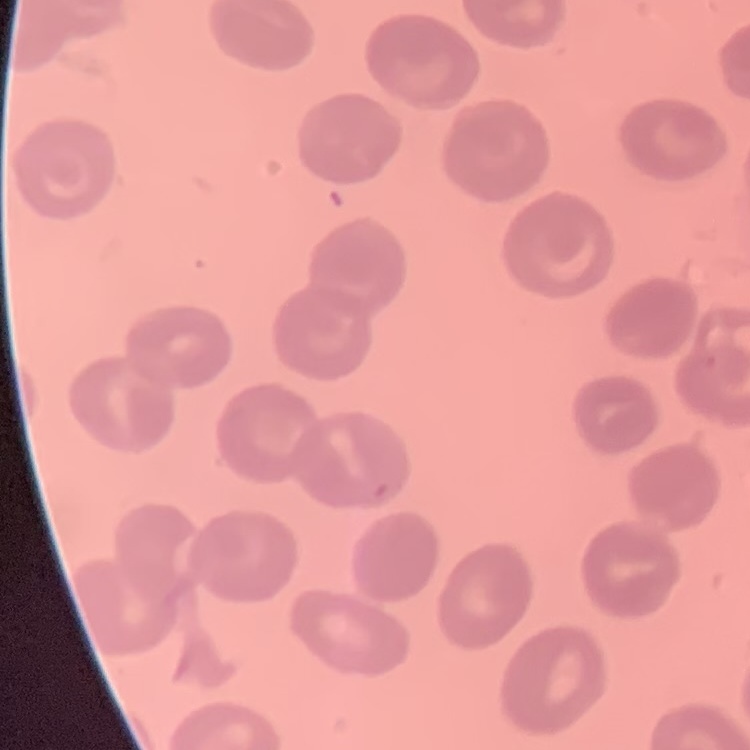

Summary:
  - Erythrocyte morphology: no rouleaux formation
  - Preparation: thin blood film
  - Stain: Field's or Giemsa
  - Image type: square crop of a larger photomicrograph